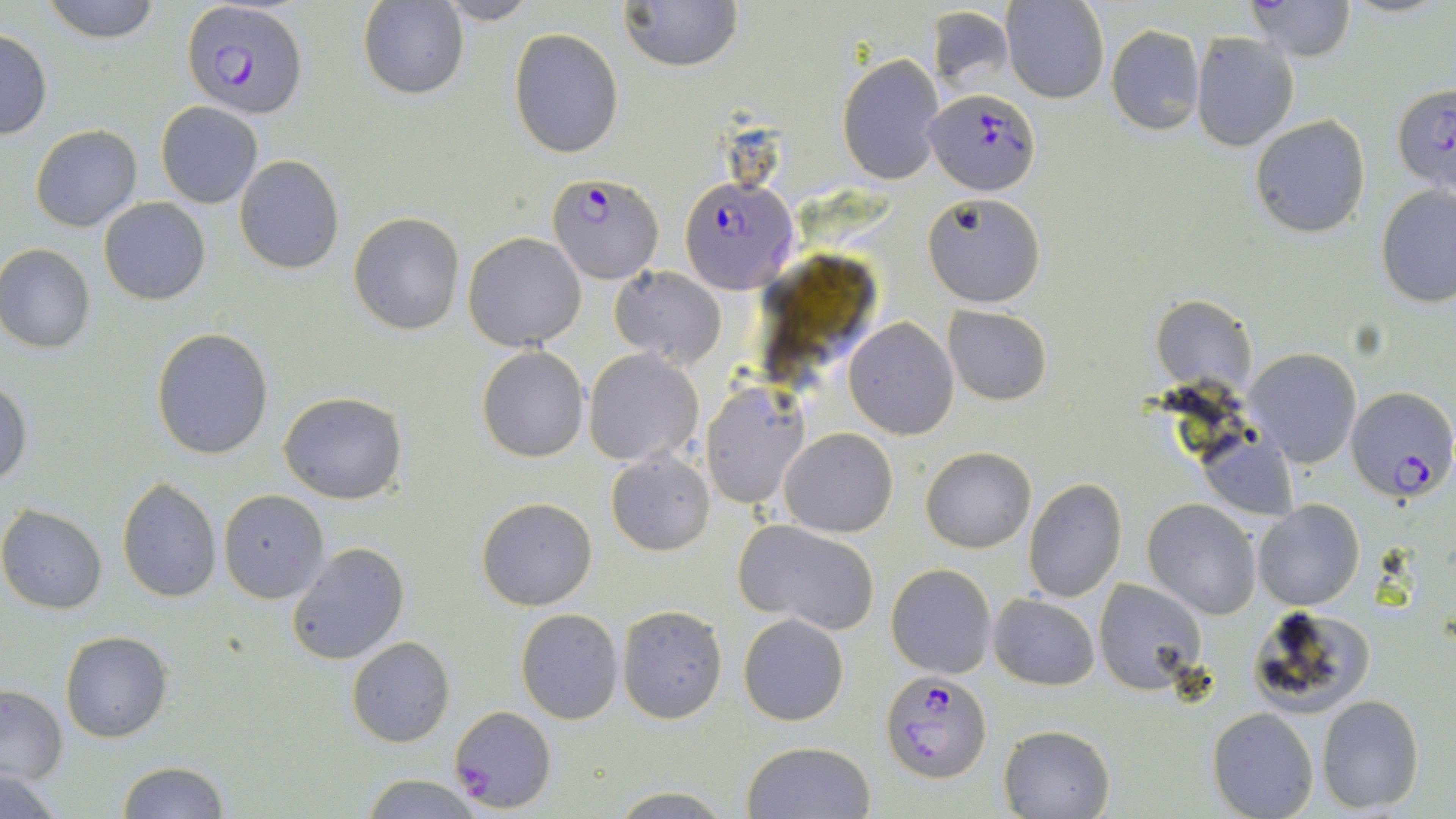
slide-level diagnosis = Plasmodium falciparum
field of view = one of a larger specimen
modality = light microscopy
Plasmodium falciparum-infected red blood cell locations = approximate bounding boxes as (x1, y1, x2, y2) in pixels: (182, 2, 308, 119), (1391, 81, 1455, 195), (926, 88, 1039, 195), (545, 171, 663, 282), (680, 174, 797, 293), (1345, 384, 1455, 502), (880, 670, 991, 783), (448, 705, 558, 812)
image size = 1456×819 pixels
magnification = 1000x
uninfected red blood cell locations = approximate bounding boxes as (x1, y1, x2, y2) in pixels: (39, 0, 163, 43), (619, 0, 743, 73), (1002, 0, 1108, 103), (358, 1, 466, 99), (433, 1, 541, 25), (1247, 1, 1357, 62), (927, 4, 1014, 94), (1106, 25, 1205, 134), (508, 28, 625, 158), (0, 31, 53, 139), (1190, 31, 1298, 150), (837, 53, 944, 185), (156, 102, 263, 208), (1248, 114, 1371, 239), (30, 124, 142, 232), (234, 155, 344, 274), (1375, 182, 1456, 308), (922, 191, 1045, 308), (99, 196, 211, 305), (349, 211, 465, 335), (463, 232, 586, 350), (0, 246, 96, 352), (612, 266, 726, 368), (1152, 293, 1256, 396), (943, 306, 1052, 405), (844, 318, 958, 438), (151, 328, 274, 461), (476, 347, 590, 462), (1245, 348, 1361, 466), (585, 349, 704, 467), (1, 378, 32, 488), (701, 383, 809, 508), (278, 391, 407, 503), (778, 428, 897, 537), (1197, 435, 1299, 522), (921, 446, 1035, 552), (606, 451, 715, 555), (116, 478, 223, 604), (1022, 478, 1127, 603), (218, 490, 330, 603), (477, 497, 597, 611), (1143, 499, 1262, 618), (1253, 499, 1364, 611), (0, 504, 106, 613), (736, 520, 880, 634), (285, 542, 409, 666), (885, 562, 996, 678), (1094, 580, 1208, 696), (988, 592, 1099, 691), (616, 604, 728, 723), (1244, 604, 1378, 720), (515, 609, 625, 725), (738, 614, 848, 726), (61, 631, 172, 743), (347, 637, 454, 747), (0, 685, 68, 784), (1317, 695, 1425, 811), (1207, 707, 1320, 819), (999, 725, 1116, 818), (741, 741, 876, 819), (116, 761, 230, 818), (0, 769, 67, 818), (360, 776, 489, 819), (605, 787, 737, 817)
preparation = thin blood smear
stain = May-Grünwald-Giemsa